Outline each blood parasite and name the species.
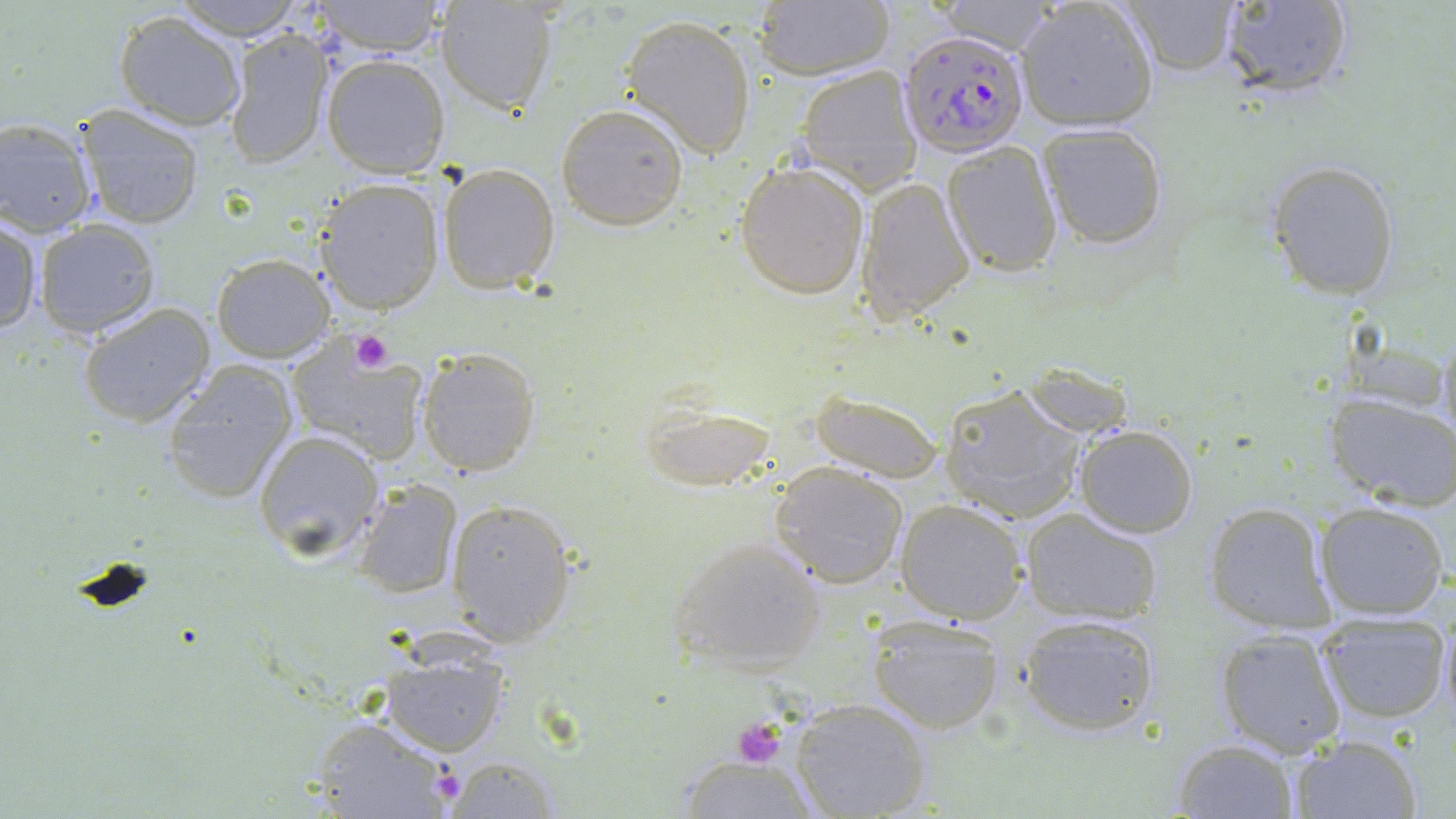

Approximate bounding boxes as (x1,y1)-(x2,y2) corner pairs in pixels.
Plasmodium falciparum-infected red blood cells: (900,29)-(1030,158).
No Plasmodium ovale, Plasmodium malariae, Plasmodium vivax, Babesia divergens, or Trypanosoma brucei observed.

Platelet locations: (349,330)-(394,374), (730,719)-(788,770). Uninfected red blood cell locations: (169,0)-(309,41), (311,0)-(448,56), (435,1)-(558,114), (935,1)-(1064,53), (1014,1)-(1158,131), (1114,1)-(1242,79), (1210,1)-(1357,101), (752,2)-(895,81), (113,10)-(248,130), (618,14)-(757,158), (223,23)-(336,169), (322,52)-(451,178), (795,64)-(922,195), (555,101)-(689,230), (74,104)-(205,229), (1,118)-(98,237), (1036,123)-(1171,248), (942,144)-(1063,277), (1265,160)-(1401,301), (735,161)-(868,297), (438,163)-(562,293), (857,176)-(976,324), (314,178)-(445,314), (0,218)-(44,336), (32,221)-(160,338), (211,254)-(337,363), (77,301)-(217,429), (1436,328)-(1456,450), (288,339)-(430,464), (416,345)-(542,475), (160,359)-(300,504), (940,385)-(1085,524), (810,390)-(943,481), (1324,392)-(1456,509), (1074,424)-(1199,536), (253,428)-(385,560), (770,462)-(908,588), (352,479)-(464,600), (444,496)-(578,646), (896,498)-(1029,624), (1201,500)-(1336,634), (1315,501)-(1451,620), (1020,508)-(1166,625), (667,533)-(827,674), (1437,596)-(1455,730), (1018,611)-(1163,737), (1317,613)-(1451,724), (866,614)-(1005,734), (1214,628)-(1349,757), (379,643)-(511,755), (788,696)-(932,819), (304,716)-(460,818), (1288,733)-(1424,819), (1171,739)-(1299,818), (676,753)-(819,818), (442,756)-(565,816). Slide-level diagnosis: Plasmodium falciparum. Image is 1456×819 pixels. Thin blood film. One field of a larger specimen. 1000x magnification. Optical microscopy. May-Grünwald-Giemsa stain.